Name the blood parasite species.
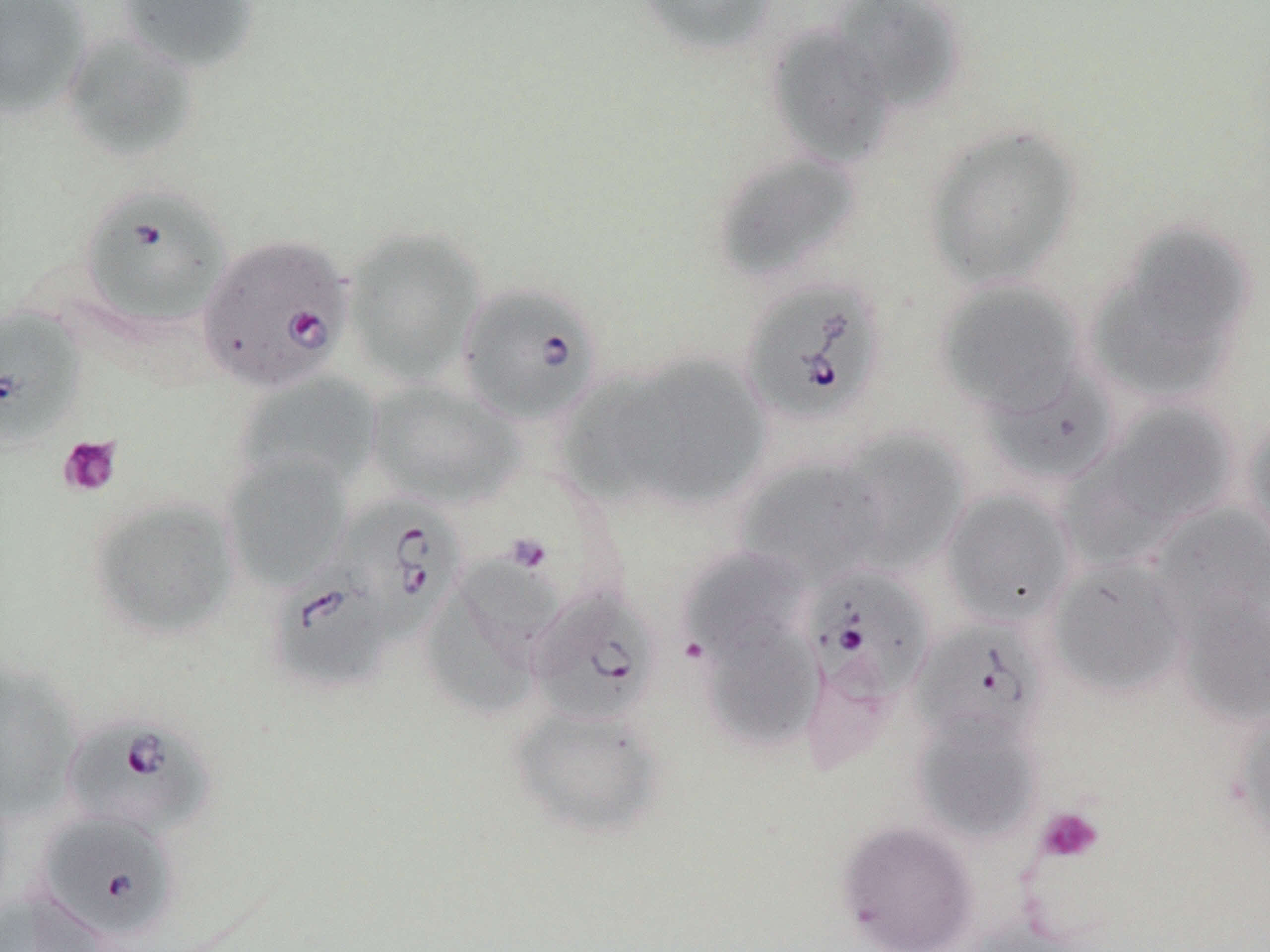

Babesia divergens.

Summary:
  - Coordinate format: approximate bounding boxes as (x1,y1)-(x2,y2) corner pairs in pixels
  - Uninfected red blood cell locations: (0,0)-(91,118), (118,0)-(260,74), (634,0)-(780,57), (829,0)-(966,112), (765,23)-(897,168), (62,31)-(200,162), (921,124)-(1084,290), (713,152)-(862,282), (341,226)-(486,386), (1094,226)-(1256,388), (933,278)-(1086,416), (617,354)-(772,510), (980,361)-(1116,486), (555,372)-(677,507), (235,374)-(379,494), (367,380)-(525,511), (1086,399)-(1241,538), (1241,415)-(1270,554), (830,429)-(971,574), (222,453)-(351,590), (737,456)-(887,588), (939,487)-(1078,628), (88,497)-(241,641), (1149,502)-(1270,629), (680,548)-(807,664), (1044,556)-(1192,698), (421,570)-(547,720), (1176,591)-(1270,727), (702,618)-(823,753), (0,660)-(80,824), (507,703)-(668,841), (1231,704)-(1270,852), (910,712)-(1043,842), (836,819)-(980,952), (2,889)-(111,951), (963,918)-(1100,952)
  - Babesia divergens-infected red blood cell locations: (77,185)-(233,332), (197,233)-(355,394), (738,277)-(889,426), (457,281)-(605,426), (0,307)-(86,450), (334,493)-(466,645), (267,561)-(394,696), (798,562)-(934,722), (526,586)-(661,726), (910,618)-(1049,750), (61,715)-(215,839), (38,813)-(177,940)
  - Platelet locations: (57,436)-(122,498), (1036,806)-(1104,863)
  - Magnification: 1000x
  - Preparation: thin blood smear
  - Image size: 1270×952 pixels
  - Modality: optical microscopy
  - Field of view: single
  - Stain: May-Grünwald-Giemsa